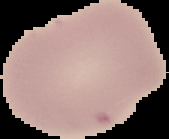
From a thin blood smear. Image is 169×139 pixels. Cell region segmented out of the field of view; the surrounding area is masked to black. Result: negative for malaria parasites.